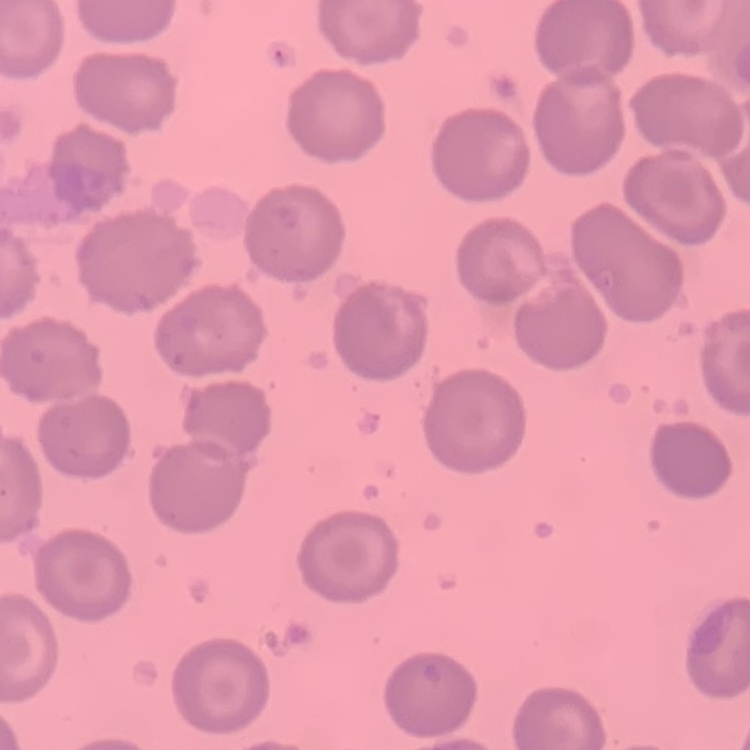
The erythrocytes exhibit no rouleaux formation. Stained with either Field's or Giemsa. Thin blood smear. Square crop of a larger photomicrograph.